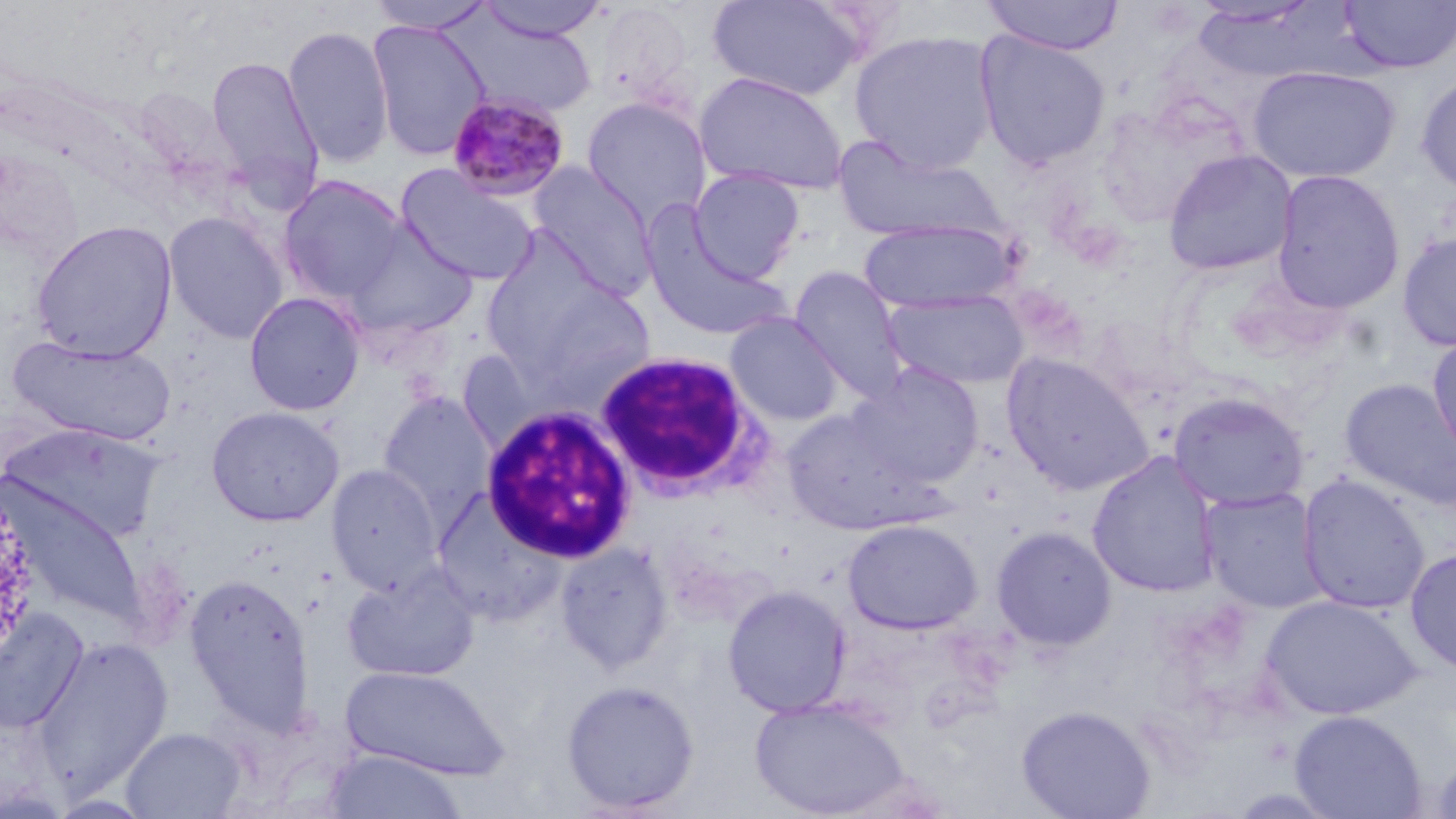
slide_level_diagnosis: Plasmodium malariae
field_of_view: single
uninfected_red_blood_cell_locations: 'approximate bounding boxes as (x1, y1, x2, y2) in pixels: (367, 0, 496, 33), (476, 0, 610, 42), (708, 0, 865, 101), (981, 0, 1125, 55), (1188, 1, 1325, 29), (1339, 1, 1456, 73), (452, 12, 600, 116), (368, 20, 490, 161), (281, 24, 395, 167), (849, 30, 1000, 174), (973, 30, 1111, 169), (206, 55, 323, 201), (1247, 66, 1401, 183), (693, 71, 849, 196), (1415, 73, 1456, 198), (133, 85, 239, 186), (582, 97, 711, 225), (835, 140, 1003, 244), (1163, 149, 1298, 277), (0, 155, 82, 257), (529, 162, 658, 299), (395, 165, 540, 287), (688, 169, 805, 283), (1271, 169, 1405, 314), (278, 175, 409, 306), (639, 209, 789, 343), (163, 210, 288, 344), (858, 218, 1017, 315), (31, 219, 177, 362), (340, 220, 478, 344), (1397, 230, 1456, 352), (788, 266, 909, 402), (501, 278, 658, 399), (883, 289, 1030, 391), (244, 292, 365, 416), (725, 313, 844, 426), (1427, 331, 1456, 469), (9, 335, 176, 446), (1000, 352, 1154, 495), (851, 364, 985, 488), (1341, 379, 1456, 509), (1168, 391, 1310, 511), (378, 392, 494, 519), (206, 406, 345, 527), (782, 408, 930, 535), (4, 424, 162, 544), (1088, 452, 1220, 599), (326, 464, 442, 594), (1298, 475, 1430, 615), (4, 483, 149, 628), (1201, 488, 1326, 613), (431, 490, 568, 626), (841, 518, 983, 635), (990, 526, 1116, 651), (555, 542, 675, 674), (1405, 547, 1456, 676), (343, 564, 481, 682), (184, 573, 315, 734), (722, 585, 852, 718), (1260, 595, 1421, 721), (0, 609, 89, 734), (32, 638, 172, 797), (340, 664, 509, 780), (561, 679, 700, 814), (749, 695, 910, 817), (1016, 705, 1155, 819), (1289, 710, 1426, 819), (121, 726, 245, 818), (322, 749, 469, 818), (1429, 751, 1456, 819)'
modality: light microscopy
preparation: thin blood smear
white_blood_cell_locations: 'approximate bounding boxes as (x1, y1, x2, y2) in pixels: (593, 348, 774, 500), (479, 404, 638, 564)'
magnification: 1000x
plasmodium_malariae_infected_red_blood_cell_locations: 'approximate bounding boxes as (x1, y1, x2, y2) in pixels: (445, 92, 570, 202)'
image_size: 1456×819 pixels
stain: May-Grünwald-Giemsa